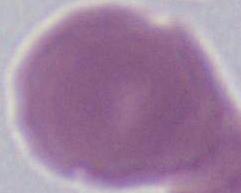
modality: photomicrograph
magnification: 1000x
identification: red blood cell